Locate every parasitized RBC.
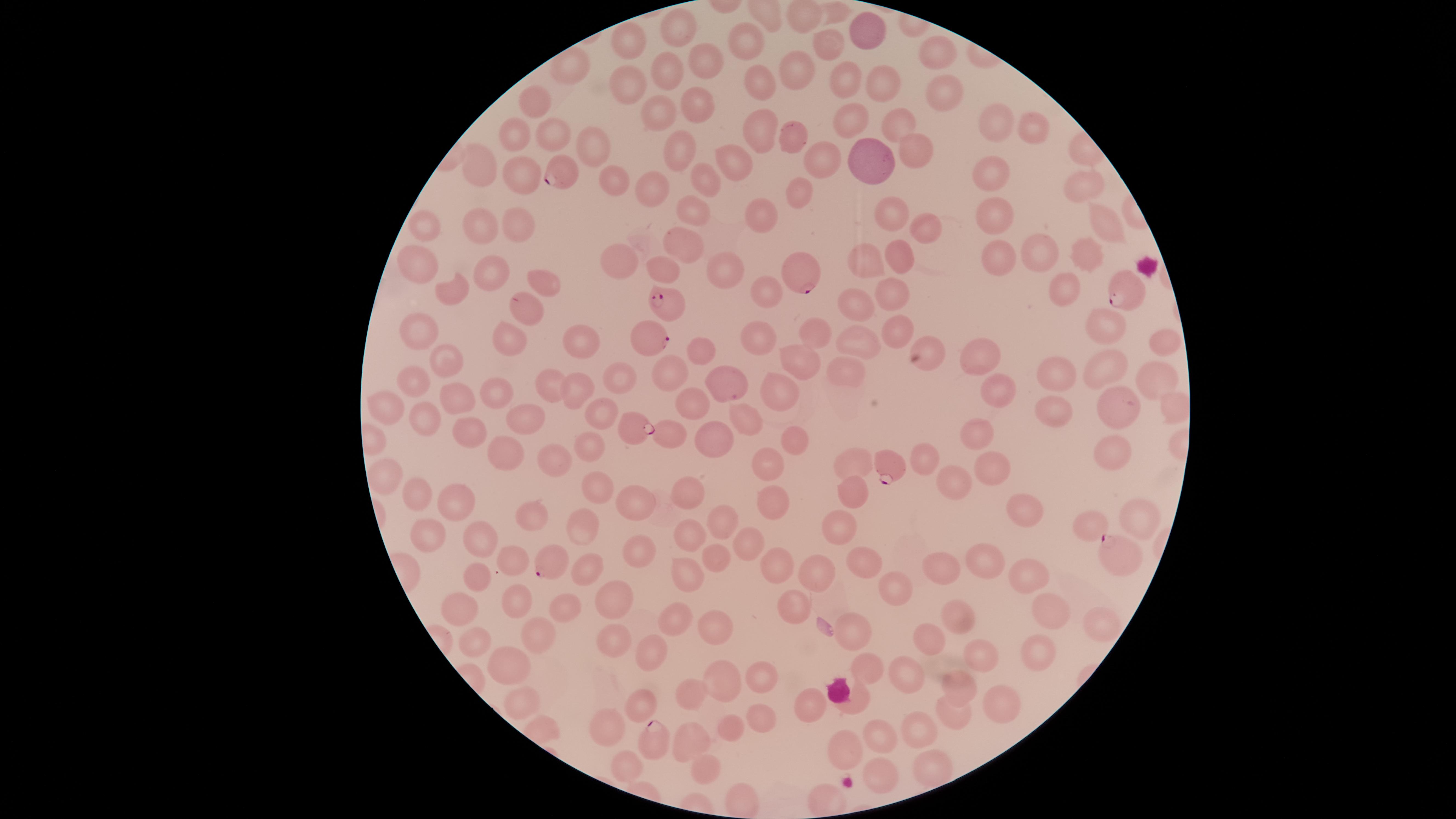
Approximate marker points, in pixels from the top-left corner.
Parasitized RBCs: (x=558, y=170), (x=807, y=274), (x=1129, y=292), (x=669, y=303), (x=656, y=340), (x=635, y=426), (x=889, y=463), (x=1121, y=551), (x=550, y=562), (x=656, y=736).

Approximate marker points, in pixels from the top-left corner. Uninfected RBCs: (x=835, y=13), (x=808, y=14), (x=674, y=30), (x=869, y=33), (x=751, y=44), (x=634, y=47), (x=835, y=50), (x=937, y=51), (x=704, y=59), (x=573, y=70), (x=801, y=75), (x=847, y=75), (x=667, y=76), (x=764, y=77), (x=886, y=81), (x=633, y=83), (x=948, y=87), (x=695, y=97), (x=535, y=107), (x=651, y=110), (x=999, y=118), (x=901, y=120), (x=855, y=123), (x=1038, y=128), (x=518, y=134), (x=771, y=135), (x=553, y=136), (x=799, y=138), (x=586, y=145), (x=681, y=152), (x=918, y=152), (x=826, y=160), (x=739, y=163), (x=874, y=165), (x=484, y=171), (x=993, y=173), (x=523, y=177), (x=613, y=180), (x=706, y=183), (x=1086, y=185), (x=650, y=189), (x=800, y=196), (x=694, y=210), (x=892, y=210), (x=996, y=211), (x=765, y=220), (x=515, y=223), (x=1110, y=224), (x=484, y=226), (x=920, y=226), (x=429, y=229), (x=683, y=241), (x=866, y=252), (x=1092, y=252), (x=1044, y=253), (x=1003, y=259), (x=903, y=260), (x=629, y=264), (x=416, y=265), (x=669, y=269), (x=494, y=272), (x=729, y=272), (x=542, y=281), (x=893, y=285), (x=765, y=288), (x=1064, y=292), (x=458, y=294), (x=527, y=308), (x=858, y=308), (x=1105, y=324), (x=892, y=325), (x=422, y=333), (x=763, y=335), (x=812, y=336), (x=512, y=338), (x=929, y=340), (x=1164, y=340), (x=863, y=344), (x=582, y=348), (x=703, y=354), (x=799, y=356), (x=988, y=359), (x=448, y=360), (x=1058, y=368), (x=1113, y=368), (x=678, y=373), (x=845, y=373), (x=1159, y=374), (x=625, y=377), (x=417, y=381), (x=730, y=381), (x=498, y=390), (x=554, y=390), (x=581, y=391), (x=787, y=391), (x=1005, y=395), (x=463, y=398), (x=694, y=401), (x=396, y=407), (x=1053, y=408), (x=1122, y=410), (x=604, y=413), (x=748, y=416), (x=422, y=419), (x=528, y=422), (x=466, y=432), (x=675, y=433), (x=976, y=433), (x=708, y=436), (x=795, y=441), (x=589, y=447), (x=501, y=453), (x=1117, y=454), (x=923, y=461), (x=551, y=464), (x=851, y=466), (x=990, y=466), (x=770, y=470), (x=389, y=477), (x=961, y=485), (x=692, y=487), (x=853, y=488), (x=601, y=490), (x=415, y=497), (x=778, y=499), (x=633, y=501), (x=462, y=503), (x=1026, y=504), (x=533, y=518), (x=1141, y=521), (x=725, y=522), (x=1096, y=525), (x=578, y=527), (x=843, y=530), (x=479, y=531), (x=431, y=538), (x=691, y=541), (x=745, y=542), (x=640, y=553), (x=514, y=555), (x=721, y=559), (x=985, y=563), (x=868, y=564), (x=777, y=565), (x=811, y=568), (x=584, y=571), (x=943, y=574), (x=1028, y=576), (x=689, y=580), (x=477, y=583), (x=898, y=588), (x=617, y=593), (x=515, y=606), (x=795, y=606), (x=1050, y=609), (x=463, y=612), (x=565, y=612), (x=960, y=616), (x=673, y=619), (x=1102, y=625), (x=715, y=626), (x=864, y=633), (x=540, y=637), (x=617, y=641), (x=934, y=642), (x=478, y=643), (x=1040, y=651), (x=649, y=653), (x=980, y=655), (x=512, y=666), (x=871, y=667), (x=755, y=673), (x=904, y=676), (x=963, y=679), (x=723, y=680), (x=810, y=699), (x=690, y=700), (x=1005, y=702), (x=521, y=703), (x=858, y=703), (x=640, y=709), (x=957, y=713), (x=757, y=719), (x=614, y=729), (x=916, y=735), (x=728, y=738), (x=877, y=743), (x=850, y=748), (x=695, y=751), (x=630, y=766), (x=931, y=769), (x=706, y=773), (x=883, y=776). Species: Plasmodium falciparum. Image is 1456×819 pixels. Single field of view. Smartphone photograph through the microscope eyepiece. Thin smear of blood. The visible region is circular. Giemsa-stained preparation.